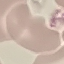

Malaria status: uninfected. Photographed with a smartphone camera at the microscope eyepiece. Giemsa stain. Thin blood film. Automatically extracted cell patch, resized to 64 × 64 pixels.